State the blood parasite species.
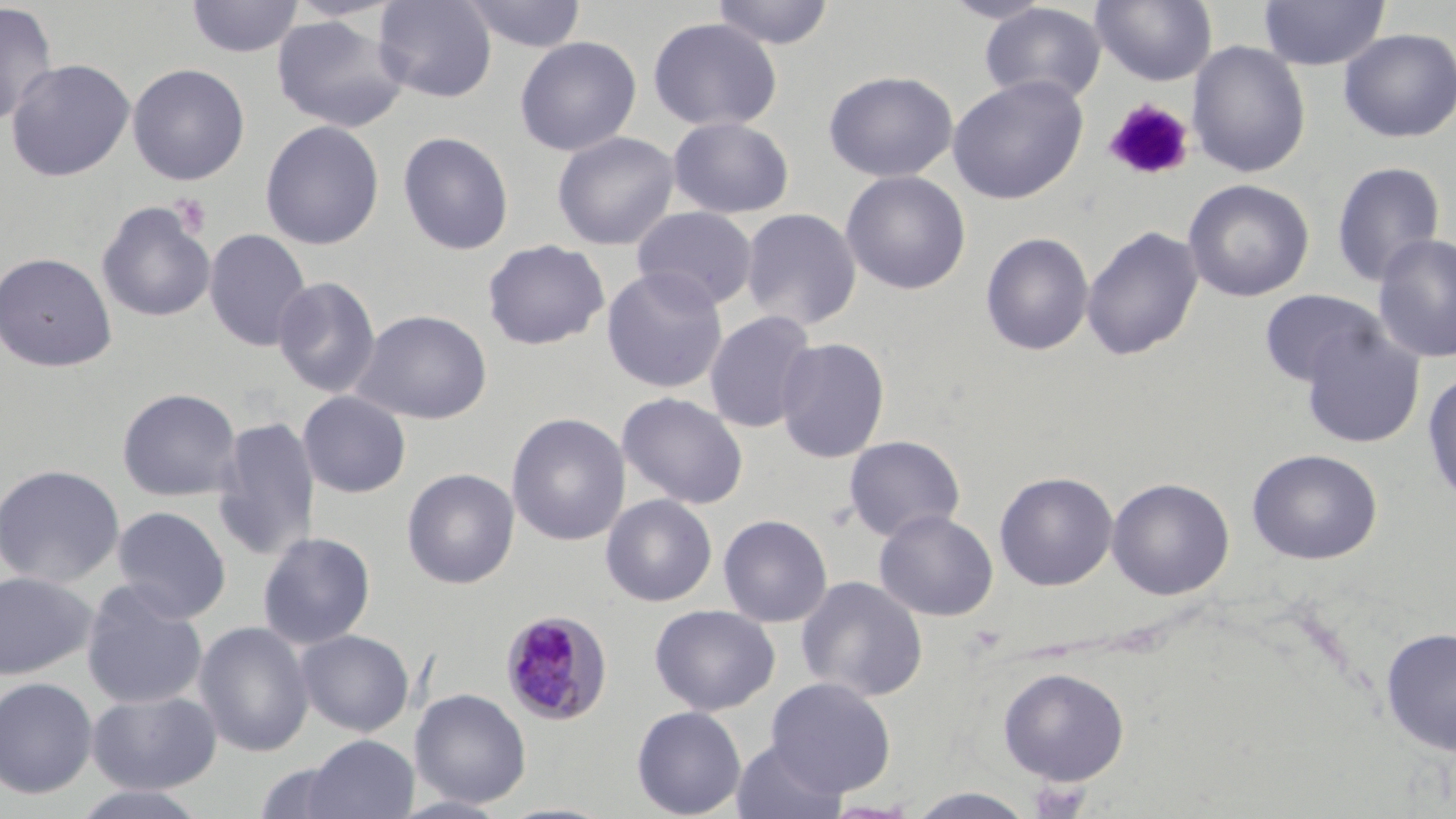

Plasmodium malariae.

Summary:
  - Coordinate format: approximate bounding boxes as (x1,y1)-(x2,y2) corner pairs in pixels
  - Uninfected red blood cell locations: (185,0)-(304,59), (282,0)-(410,23), (373,0)-(497,103), (457,0)-(588,53), (709,0)-(837,50), (940,0)-(1057,24), (1091,0)-(1217,86), (1258,0)-(1390,70), (0,3)-(58,128), (980,3)-(1107,105), (271,15)-(408,133), (647,17)-(783,132), (1338,28)-(1456,142), (515,36)-(642,156), (1187,41)-(1311,178), (5,58)-(135,182), (127,63)-(250,185), (823,70)-(959,182), (947,76)-(1089,204), (667,116)-(794,219), (259,120)-(385,250), (398,131)-(514,255), (552,131)-(680,251), (1329,161)-(1447,287), (839,170)-(972,295), (1182,178)-(1314,301), (97,202)-(215,323), (631,206)-(758,312), (740,207)-(862,331), (1081,224)-(1204,362), (204,228)-(312,352), (980,231)-(1095,356), (1371,232)-(1456,364), (482,239)-(610,350), (0,251)-(117,372), (601,266)-(729,395), (272,275)-(380,399), (1259,289)-(1384,388), (352,309)-(492,425), (704,309)-(819,433), (1299,323)-(1426,449), (775,337)-(890,463), (1422,369)-(1456,509), (117,387)-(241,501), (298,391)-(411,498), (617,392)-(749,509), (507,405)-(751,529), (506,412)-(631,547), (213,415)-(320,562), (843,435)-(965,542), (1246,448)-(1383,564), (0,463)-(125,589), (401,468)-(520,589), (994,471)-(1118,591), (1106,477)-(1235,600), (601,494)-(718,607), (111,505)-(231,623), (873,509)-(999,621), (718,514)-(833,628), (257,531)-(376,649), (0,570)-(97,680), (795,575)-(929,703), (81,580)-(208,710), (649,604)-(780,716), (194,621)-(314,758), (1379,626)-(1456,756), (296,629)-(414,736), (997,666)-(1130,786), (0,676)-(98,800), (765,677)-(896,798), (410,688)-(531,808), (86,689)-(222,795), (631,705)-(746,818), (303,735)-(417,819), (730,740)-(848,819), (66,785)-(213,819), (906,787)-(1037,818)
  - Plasmodium malariae-infected red blood cell locations: (500,610)-(612,725)
  - Platelet locations: (1103,98)-(1196,183), (170,193)-(211,239)
  - Field of view: one of a larger specimen
  - Magnification: 1000x
  - Modality: light microscopy
  - Stain: May-Grünwald-Giemsa
  - Image size: 1456×819 pixels
  - Preparation: thin blood film